Report the malaria status of this cell.
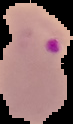

It is parasitized.

preparation = thin blood film
image size = 73×124 pixels
image type = segmented cell region with the area outside set to black